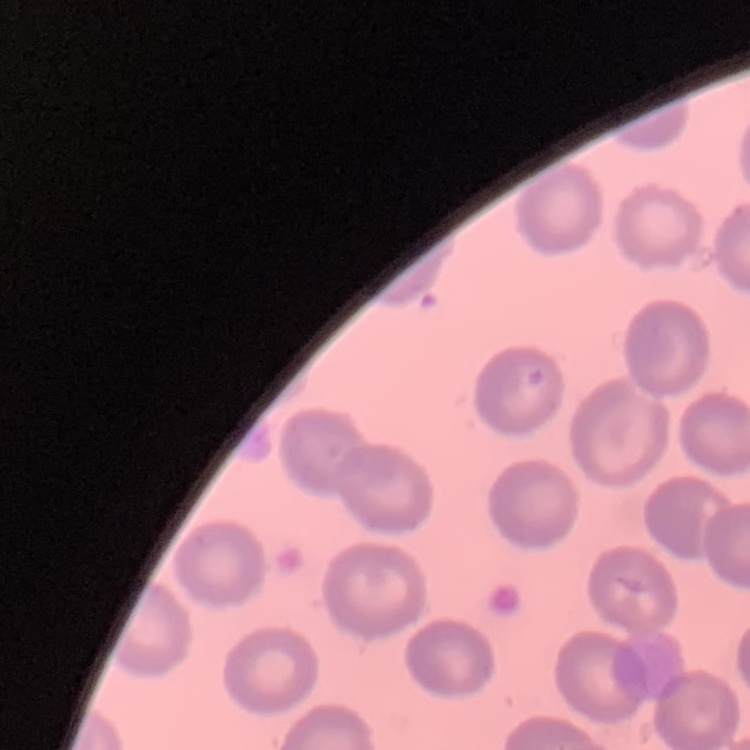 The red blood cells exhibit no rouleaux formation. Thin blood film. Square crop of a larger photomicrograph. Stained with either Field's or Giemsa.